Assess this cell for malaria.
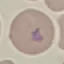

It is uninfected.

Automatically extracted cell patch, resized to 64 × 64 pixels. Acquired by smartphone through the microscope eyepiece. Thin blood film. Giemsa-stained preparation.